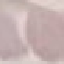

result = negative for malaria parasites
image type = automatically extracted cell patch, resized to 64 × 64 pixels
stain = Giemsa
preparation = thin blood smear
capture = smartphone through the microscope eyepiece